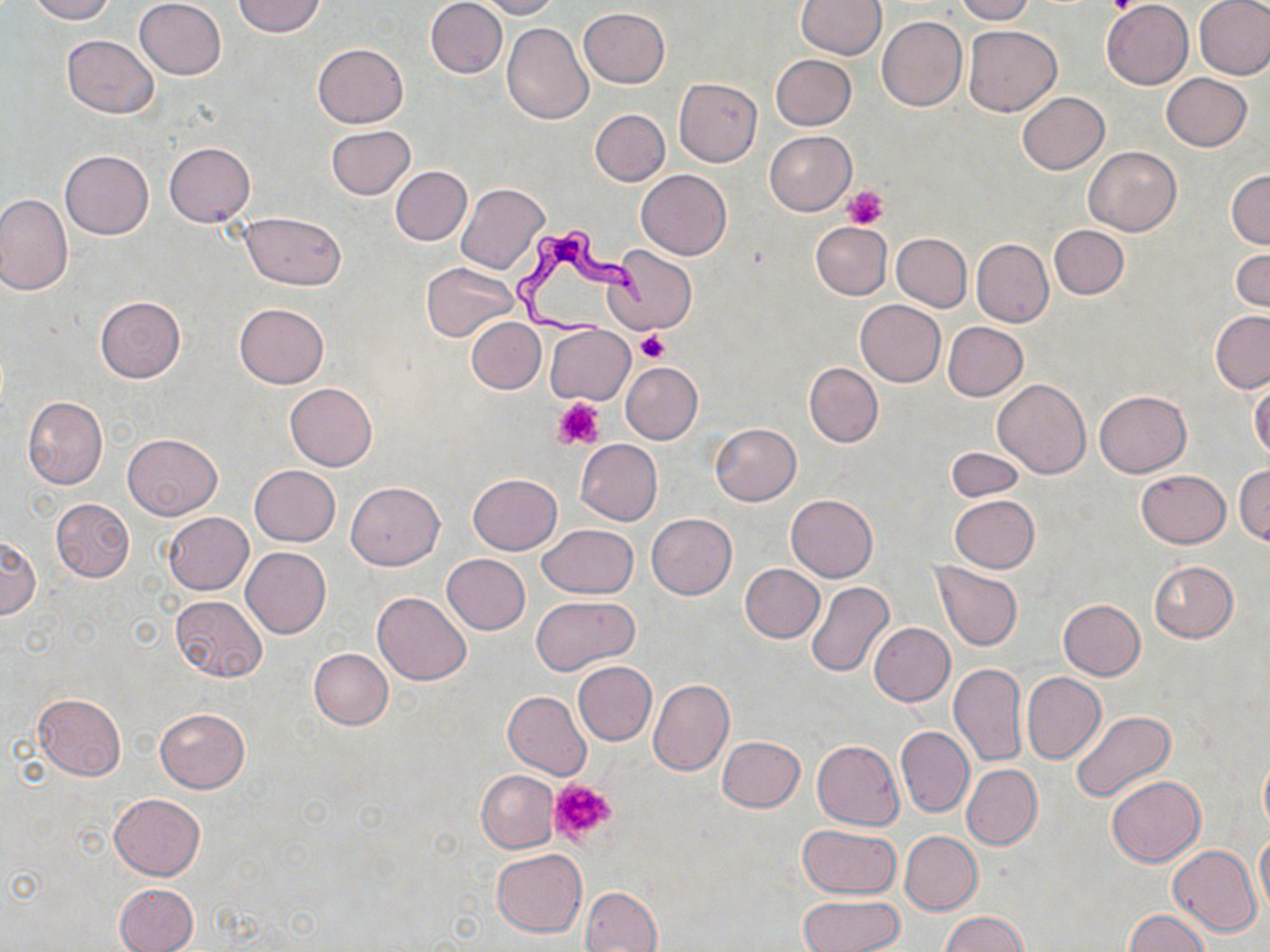

slide-level diagnosis = Trypanosoma brucei
modality = optical microscopy
Trypanosoma brucei locations = approximate bounding boxes as (x1, y1, x2, y2) in pixels: (509, 226, 654, 339)
preparation = thin blood film
magnification = 1000x
field of view = one of a larger specimen
uninfected red blood cell locations = approximate bounding boxes as (x1, y1, x2, y2) in pixels: (26, 0, 116, 23), (134, 0, 226, 80), (234, 0, 325, 37), (425, 0, 507, 78), (478, 0, 560, 19), (797, 0, 886, 59), (953, 0, 1035, 23), (1102, 0, 1193, 88), (1195, 1, 1270, 80), (578, 7, 669, 88), (876, 15, 968, 111), (502, 22, 593, 123), (962, 23, 1062, 116), (61, 34, 161, 118), (312, 43, 408, 128), (772, 54, 857, 130), (1162, 73, 1251, 150), (674, 77, 763, 167), (1017, 91, 1109, 174), (590, 109, 669, 186), (326, 125, 415, 199), (765, 131, 856, 215), (164, 143, 255, 227), (1084, 147, 1180, 236), (59, 150, 153, 240), (391, 166, 472, 246), (637, 170, 732, 260), (1227, 170, 1270, 249), (456, 182, 549, 274), (0, 194, 73, 296), (243, 212, 346, 288), (811, 221, 892, 300), (1050, 225, 1128, 299), (892, 233, 971, 311), (972, 239, 1052, 326), (605, 244, 696, 335), (1231, 249, 1270, 312), (422, 263, 520, 343), (95, 296, 186, 382), (855, 301, 945, 387), (234, 303, 329, 388), (1210, 311, 1270, 392), (466, 317, 545, 394), (942, 321, 1027, 401), (545, 325, 634, 405), (621, 362, 702, 444), (804, 363, 883, 447), (993, 378, 1090, 479), (1249, 379, 1269, 460), (285, 383, 377, 470), (1094, 391, 1191, 477), (22, 397, 108, 488), (710, 423, 801, 505), (123, 433, 221, 518), (576, 439, 662, 525), (945, 448, 1025, 502), (1234, 464, 1270, 544), (249, 465, 340, 545), (1136, 470, 1230, 548), (467, 473, 562, 555), (346, 482, 444, 570), (785, 494, 877, 582), (950, 495, 1039, 573), (51, 498, 134, 583), (164, 512, 253, 595), (647, 513, 737, 599), (538, 525, 638, 598), (0, 536, 39, 619), (242, 547, 331, 638), (441, 554, 530, 634), (1149, 561, 1238, 643), (740, 563, 824, 642), (932, 563, 1022, 651), (806, 581, 894, 678), (373, 592, 471, 686), (169, 595, 267, 682), (532, 596, 638, 673), (1057, 599, 1145, 681), (869, 622, 955, 705), (309, 648, 393, 729), (573, 661, 656, 745), (949, 663, 1027, 767), (1021, 672, 1107, 764), (648, 678, 733, 776), (503, 690, 591, 780), (33, 693, 125, 781), (156, 708, 249, 792), (1070, 711, 1175, 802), (895, 726, 973, 818), (718, 736, 803, 812), (812, 740, 904, 829), (1259, 747, 1270, 839), (962, 764, 1042, 850), (476, 770, 559, 853), (1105, 775, 1204, 867), (109, 793, 204, 880), (798, 825, 902, 898), (899, 831, 981, 915), (1255, 833, 1270, 916), (1168, 845, 1262, 937), (491, 848, 587, 937), (114, 882, 198, 952), (580, 886, 661, 952), (797, 895, 905, 952), (1123, 910, 1211, 952), (943, 912, 1026, 951)
platelet locations = approximate bounding boxes as (x1, y1, x2, y2) in pixels: (1106, 0, 1142, 16), (843, 186, 888, 228), (636, 329, 669, 363), (554, 396, 606, 450), (548, 778, 619, 846)
image size = 1270×952 pixels
stain = May-Grünwald-Giemsa